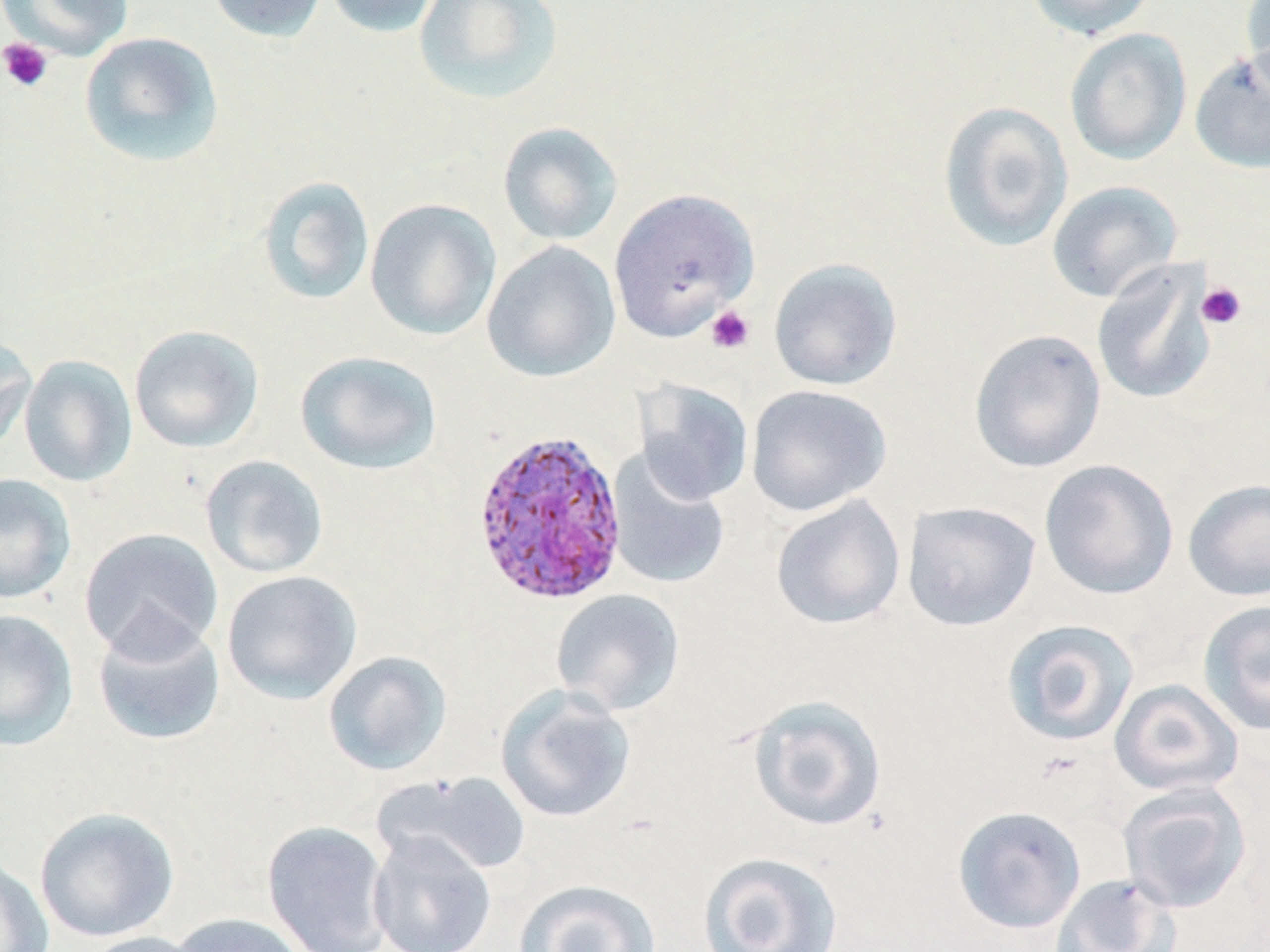

Summary:
  - Coordinate format: approximate bounding boxes as named x1/y1/x2/y2 corners in pixels
  - Plasmodium ovale-infected red blood cell locations: (x1=470, y1=426, x2=629, y2=608)
  - Platelet locations: (x1=0, y1=37, x2=53, y2=93), (x1=1197, y1=282, x2=1246, y2=329), (x1=705, y1=305, x2=755, y2=354)
  - Uninfected red blood cell locations: (x1=1, y1=0, x2=134, y2=60), (x1=205, y1=0, x2=329, y2=43), (x1=324, y1=0, x2=442, y2=38), (x1=413, y1=0, x2=564, y2=106), (x1=1025, y1=0, x2=1158, y2=40), (x1=1241, y1=0, x2=1270, y2=103), (x1=1064, y1=28, x2=1192, y2=165), (x1=79, y1=31, x2=224, y2=167), (x1=1190, y1=49, x2=1270, y2=174), (x1=937, y1=101, x2=1074, y2=252), (x1=497, y1=122, x2=624, y2=246), (x1=257, y1=176, x2=376, y2=307), (x1=1046, y1=180, x2=1183, y2=303), (x1=609, y1=187, x2=760, y2=341), (x1=365, y1=198, x2=502, y2=341), (x1=482, y1=240, x2=621, y2=383), (x1=768, y1=258, x2=902, y2=390), (x1=1091, y1=261, x2=1216, y2=407), (x1=128, y1=324, x2=264, y2=453), (x1=968, y1=328, x2=1106, y2=473), (x1=0, y1=333, x2=36, y2=455), (x1=296, y1=351, x2=442, y2=475), (x1=18, y1=355, x2=138, y2=487), (x1=634, y1=380, x2=754, y2=505), (x1=746, y1=384, x2=892, y2=516), (x1=606, y1=452, x2=731, y2=590), (x1=199, y1=455, x2=329, y2=579), (x1=1039, y1=458, x2=1179, y2=600), (x1=0, y1=473, x2=77, y2=604), (x1=1183, y1=478, x2=1270, y2=602), (x1=770, y1=494, x2=906, y2=630), (x1=902, y1=501, x2=1041, y2=631), (x1=79, y1=527, x2=224, y2=662), (x1=221, y1=570, x2=362, y2=705), (x1=550, y1=588, x2=685, y2=716), (x1=1197, y1=599, x2=1270, y2=735), (x1=0, y1=609, x2=79, y2=751), (x1=92, y1=614, x2=226, y2=747), (x1=1000, y1=618, x2=1140, y2=747), (x1=323, y1=651, x2=452, y2=776), (x1=1109, y1=679, x2=1244, y2=797), (x1=495, y1=686, x2=636, y2=823), (x1=745, y1=694, x2=888, y2=832), (x1=376, y1=770, x2=532, y2=877), (x1=1117, y1=782, x2=1252, y2=913), (x1=952, y1=805, x2=1086, y2=934), (x1=34, y1=806, x2=180, y2=943), (x1=262, y1=819, x2=393, y2=952), (x1=367, y1=829, x2=497, y2=952), (x1=698, y1=850, x2=844, y2=951), (x1=0, y1=857, x2=54, y2=952), (x1=1049, y1=873, x2=1179, y2=952), (x1=512, y1=879, x2=661, y2=952), (x1=168, y1=913, x2=309, y2=952), (x1=79, y1=932, x2=206, y2=952)
  - Slide-level diagnosis: Plasmodium ovale
  - Modality: optical microscopy
  - Field of view: single
  - Image size: 1270×952 pixels
  - Magnification: 1000x
  - Preparation: thin blood film
  - Stain: May-Grünwald-Giemsa